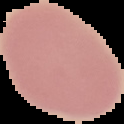
Summary:
  - Image size: 124×124 pixels
  - Image type: cell region segmented out of the field of view; surrounding area masked to black
  - Preparation: thin blood smear
  - Malaria status: uninfected